Report the malaria status of this cell.
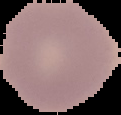
It is uninfected.

Image is 121×115 pixels. Cell region segmented out of the field of view; the surrounding area is masked to black. From a thin blood smear.